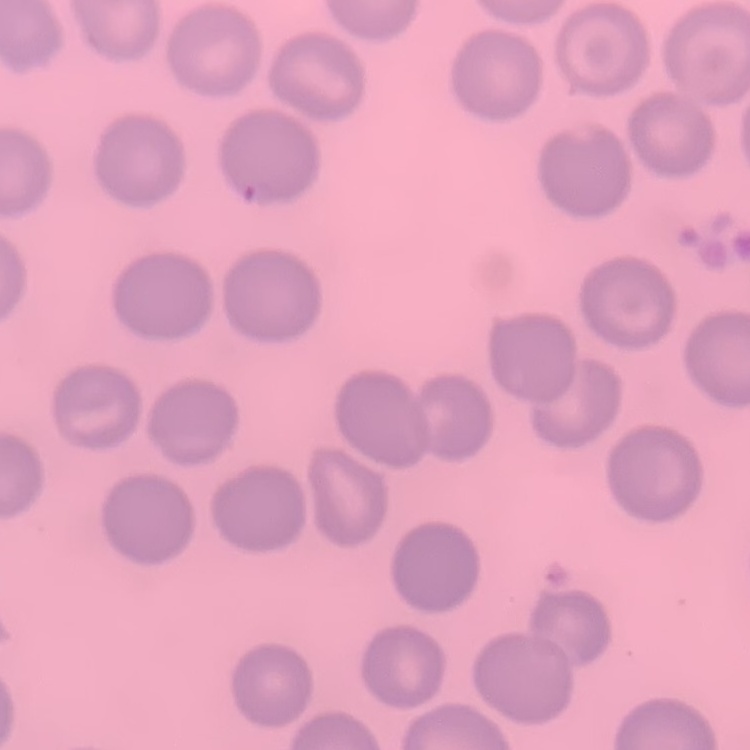

The red blood cells exhibit no rouleaux formation. Stained with either Field's or Giemsa. One tile cut from a larger photomicrograph. Thin peripheral smear.